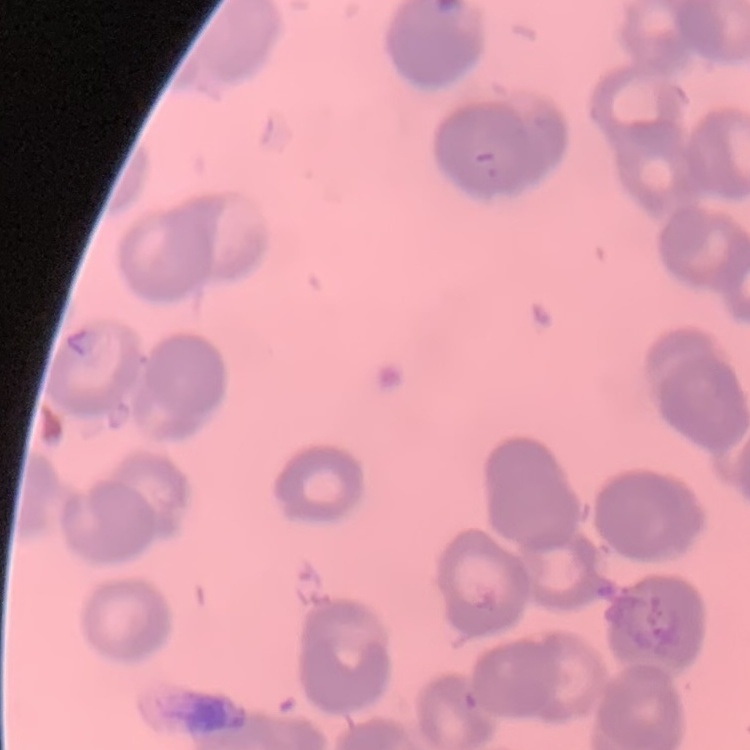

red blood cell morphology = rouleaux formation
image type = one tile cut from a larger photomicrograph
preparation = thin blood film
stain = Field's or Giemsa